Report the malaria status of this cell.
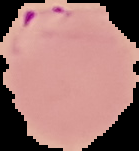

Parasitized.

image_size: 139×151 pixels
preparation: thin blood smear
image_type: segmented cell region on a black background